Name the parasite shown.
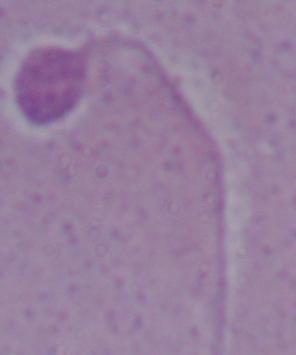

Leishmania.

Micrograph. Captured at 1000x magnification.